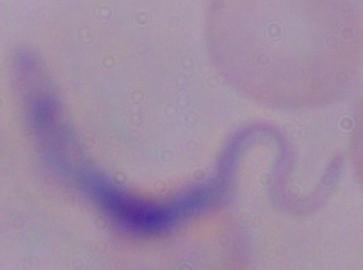 Photomicrograph. 1000x magnification. A trypanosome is seen.